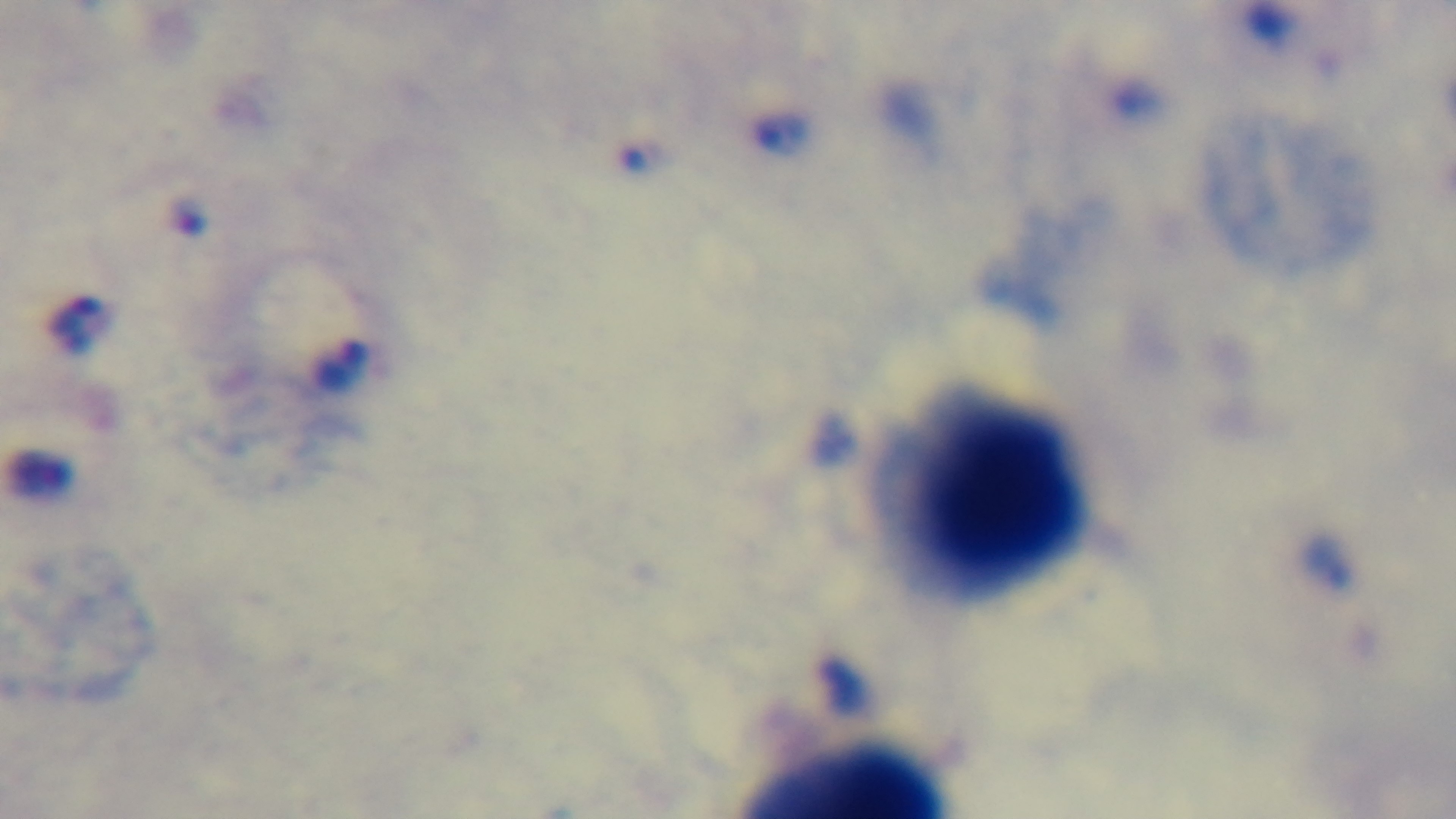
stain: Giemsa
malaria_status: positive
capture: mounted 4K digital camera
modality: light microscopy
objective: 100x oil immersion
preparation: thick blood film
field_of_view: single